Locate and identify every blood parasite.
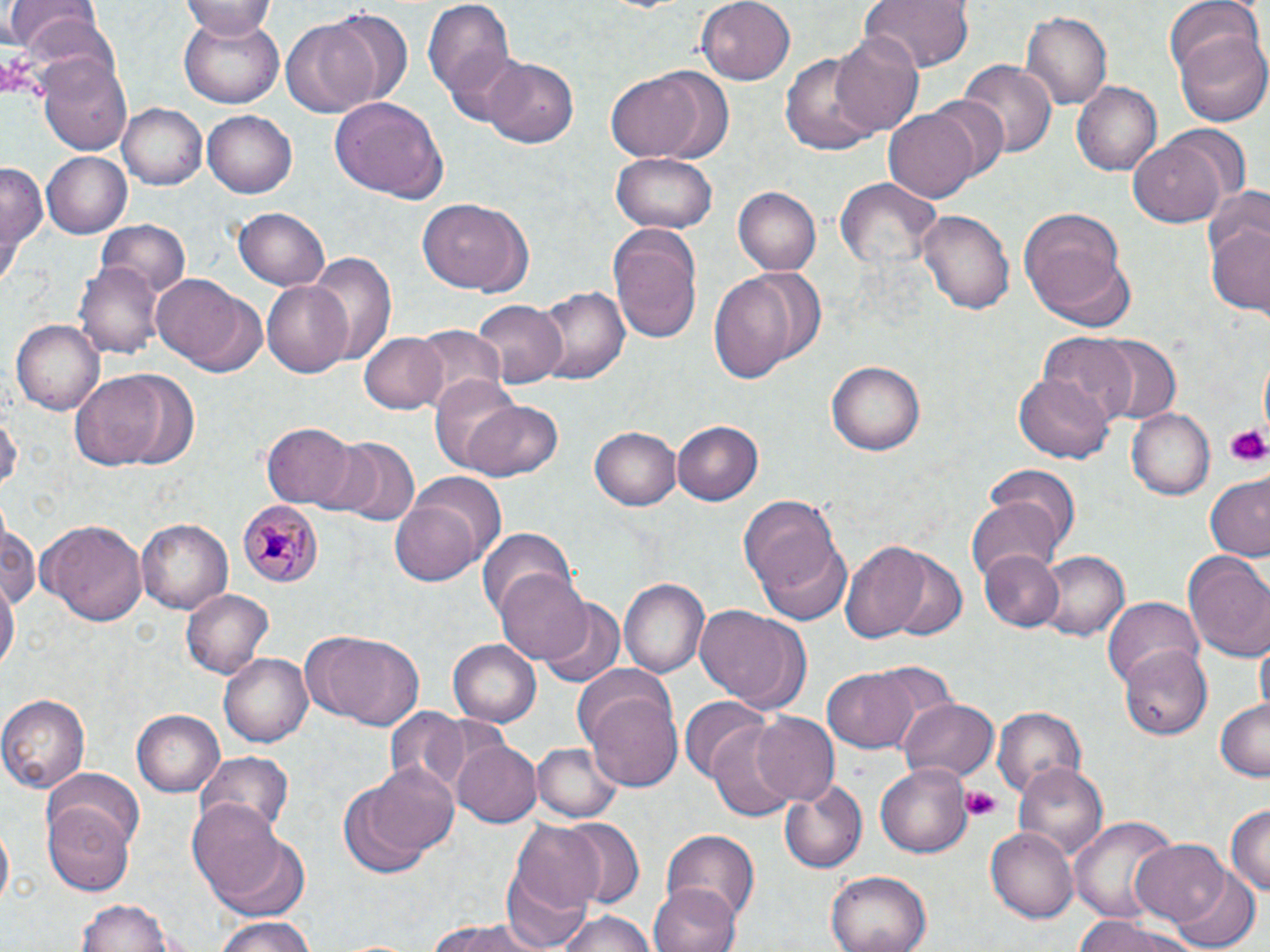
Approximate bounding boxes as [x1, y1, x2, y2] in pixels.
Plasmodium malariae-infected red blood cells: [240, 498, 321, 590].
No Plasmodium falciparum, Plasmodium ovale, Plasmodium vivax, Babesia divergens, or Trypanosoma brucei observed.

Platelet locations: [1224, 424, 1267, 464], [961, 786, 1002, 818]. Uninfected red blood cell locations: [422, 0, 517, 103], [698, 0, 798, 82], [856, 0, 976, 72], [1164, 0, 1263, 84], [8, 1, 102, 58], [181, 1, 279, 40], [324, 7, 413, 110], [1019, 10, 1113, 112], [178, 15, 285, 109], [281, 20, 379, 119], [1174, 28, 1269, 125], [832, 30, 924, 137], [439, 45, 534, 130], [781, 50, 884, 154], [39, 52, 134, 158], [483, 56, 580, 150], [958, 60, 1055, 160], [606, 69, 708, 162], [1072, 81, 1162, 175], [328, 96, 449, 202], [923, 97, 1010, 181], [119, 104, 207, 189], [883, 108, 981, 204], [202, 111, 298, 198], [1130, 135, 1229, 228], [42, 151, 133, 237], [612, 151, 717, 236], [1, 160, 49, 280], [834, 176, 939, 269], [1203, 185, 1270, 264], [734, 186, 821, 276], [416, 199, 532, 296], [231, 207, 331, 291], [917, 207, 1014, 315], [1020, 208, 1125, 314], [1206, 215, 1270, 319], [98, 219, 190, 295], [608, 222, 704, 344], [1033, 249, 1136, 333], [308, 251, 397, 366], [75, 259, 164, 362], [709, 270, 803, 387], [154, 278, 262, 374], [261, 279, 355, 376], [531, 285, 630, 386], [473, 298, 566, 385], [10, 317, 104, 413], [412, 326, 507, 406], [358, 330, 448, 413], [1038, 331, 1139, 424], [1091, 334, 1182, 424], [828, 360, 927, 455], [69, 371, 178, 469], [1016, 371, 1114, 463], [426, 374, 528, 471], [460, 399, 562, 482], [1127, 407, 1216, 499], [0, 409, 20, 500], [673, 420, 764, 507], [260, 422, 361, 510], [592, 425, 684, 511], [332, 438, 418, 524], [985, 462, 1083, 553], [407, 473, 506, 565], [1203, 477, 1270, 561], [741, 494, 852, 623], [966, 495, 1064, 591], [390, 499, 484, 586], [0, 513, 39, 617], [37, 516, 147, 624], [136, 518, 233, 613], [479, 525, 578, 624], [865, 543, 970, 641], [1181, 548, 1270, 660], [978, 549, 1065, 632], [1040, 551, 1128, 641], [495, 570, 592, 666], [619, 577, 711, 681], [1, 579, 18, 679], [182, 588, 274, 677], [1103, 597, 1204, 689], [540, 600, 625, 688], [695, 606, 804, 712], [304, 628, 425, 730], [1256, 636, 1268, 723], [449, 641, 540, 725], [1120, 647, 1213, 741], [220, 653, 314, 748], [865, 661, 961, 751], [820, 668, 918, 753], [582, 685, 686, 791], [0, 694, 89, 794], [679, 697, 771, 779], [898, 698, 997, 785], [1215, 699, 1269, 782], [992, 706, 1086, 800], [382, 707, 469, 802], [133, 710, 223, 798], [751, 713, 840, 807], [708, 720, 801, 823], [453, 739, 542, 828], [532, 743, 623, 823], [196, 749, 295, 837], [1011, 759, 1108, 863], [359, 761, 460, 857], [875, 764, 974, 858], [44, 768, 145, 852], [780, 781, 868, 873], [339, 784, 436, 878], [187, 799, 286, 902], [42, 804, 135, 895], [1225, 805, 1269, 898], [1070, 815, 1180, 926], [550, 816, 646, 911], [511, 820, 612, 918], [986, 826, 1079, 923], [661, 828, 759, 920], [214, 835, 310, 922], [1131, 839, 1231, 928], [1170, 868, 1260, 951], [499, 870, 595, 950], [827, 870, 931, 952], [217, 879, 310, 952], [648, 885, 740, 952], [76, 897, 179, 952], [552, 909, 658, 952], [1073, 916, 1196, 952], [210, 917, 318, 952], [425, 917, 548, 952]. Slide-level diagnosis: Plasmodium malariae. Thin blood film. 1000x magnification. Image is 1270×952 pixels. Light microscopy. May-Grünwald-Giemsa stain. Single field of view.